State which parasite is depicted.
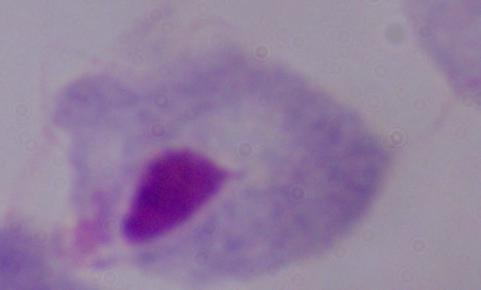
A trichomonad.

Micrograph. 1000x magnification.